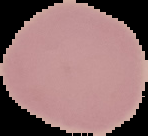

image_type: segmented cell region with the area outside set to black
image_size: 148×136 pixels
preparation: thin blood smear
result: negative for Plasmodium parasites